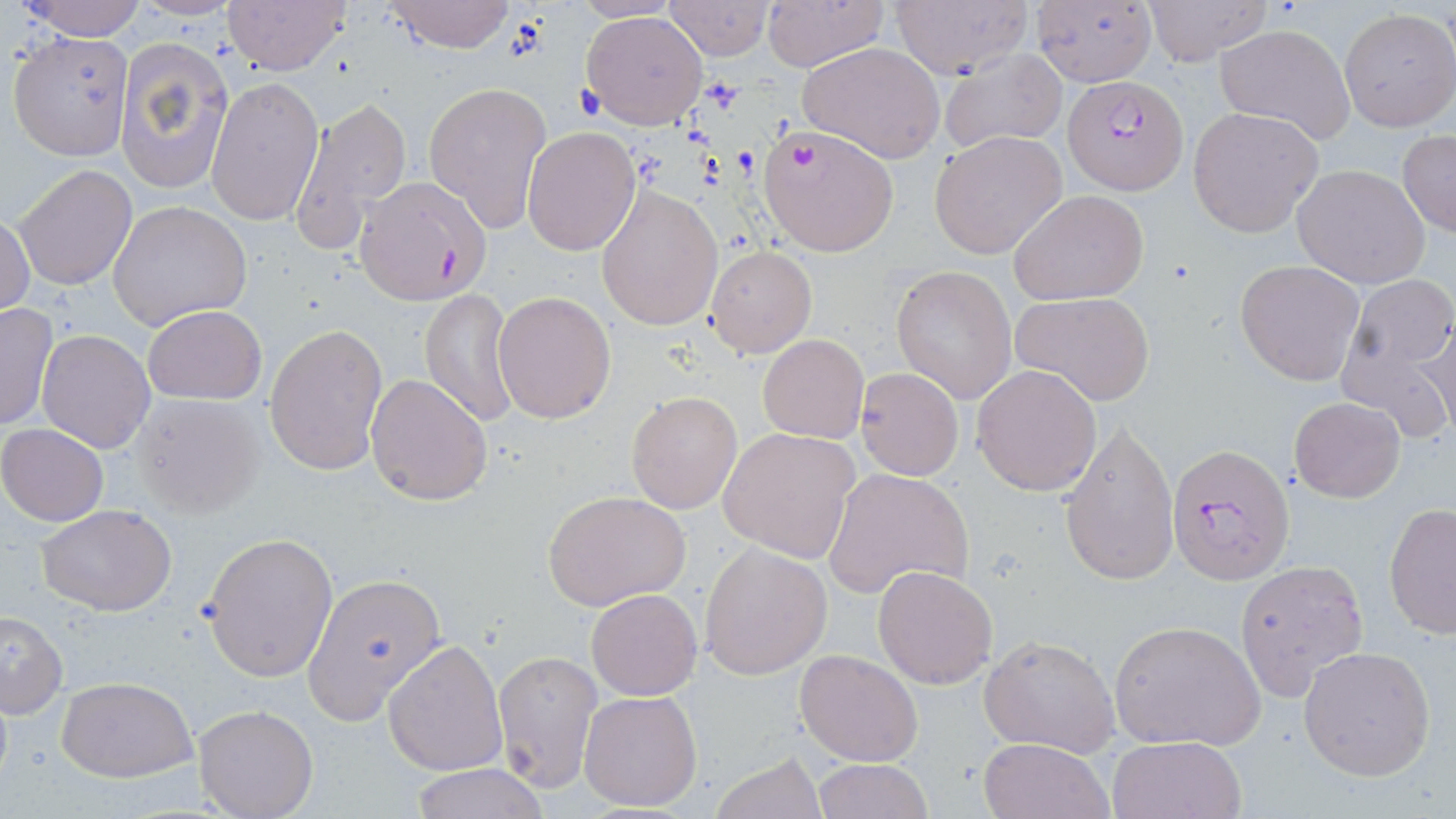

Summary:
  - Coordinate format: approximate bounding boxes as (x1,y1)-(x2,y2) corner pairs in pixels
  - Platelet locations: (505,16)-(549,61), (571,83)-(607,121)
  - Plasmodium falciparum-infected red blood cell locations: (1063,73)-(1189,194), (356,176)-(492,304), (1166,441)-(1295,586)
  - Uninfected red blood cell locations: (19,0)-(149,41), (380,0)-(517,53), (760,0)-(888,71), (1141,0)-(1272,66), (221,1)-(351,76), (661,1)-(774,61), (1029,1)-(1158,84), (890,2)-(1032,78), (1337,8)-(1455,132), (579,9)-(710,130), (1213,23)-(1356,145), (5,32)-(132,160), (113,36)-(233,195), (798,41)-(947,165), (938,49)-(1068,156), (206,75)-(323,227), (422,79)-(552,234), (288,95)-(413,250), (1188,107)-(1323,238), (756,123)-(899,257), (522,128)-(641,257), (929,130)-(1067,258), (1397,131)-(1456,237), (1292,164)-(1431,288), (13,165)-(135,291), (594,183)-(723,330), (1009,190)-(1150,306), (107,201)-(253,332), (1,209)-(36,318), (705,244)-(817,358), (1235,260)-(1366,385), (891,265)-(1018,402), (1333,278)-(1456,442), (420,287)-(520,428), (1011,290)-(1156,406), (493,292)-(616,425), (0,302)-(58,432), (141,305)-(267,404), (1416,315)-(1455,438), (403,323)-(514,490), (264,324)-(388,478), (37,329)-(156,453), (757,334)-(869,442), (972,365)-(1103,497), (855,366)-(963,481), (365,372)-(493,506), (626,391)-(742,513), (130,395)-(264,519), (1289,396)-(1405,502), (1058,418)-(1179,588), (1,423)-(108,526), (719,428)-(859,563), (822,468)-(973,599), (543,491)-(692,612), (1384,502)-(1456,639), (37,503)-(178,615), (202,531)-(338,682), (700,543)-(833,679), (1234,561)-(1373,705), (873,565)-(999,689), (302,574)-(449,724), (586,588)-(702,700), (1,611)-(68,718), (1110,618)-(1268,754), (979,634)-(1120,756), (383,639)-(508,776), (1298,645)-(1436,781), (492,647)-(604,794), (795,648)-(924,766), (57,677)-(197,783), (579,689)-(704,812), (193,704)-(319,819), (1106,735)-(1246,819), (978,736)-(1113,819), (708,752)-(829,819), (811,758)-(932,819), (408,764)-(549,819)
  - Slide-level diagnosis: Plasmodium falciparum
  - Magnification: 1000x
  - Image size: 1456×819 pixels
  - Preparation: thin blood smear
  - Field of view: single
  - Stain: May-Grünwald-Giemsa
  - Modality: optical microscopy